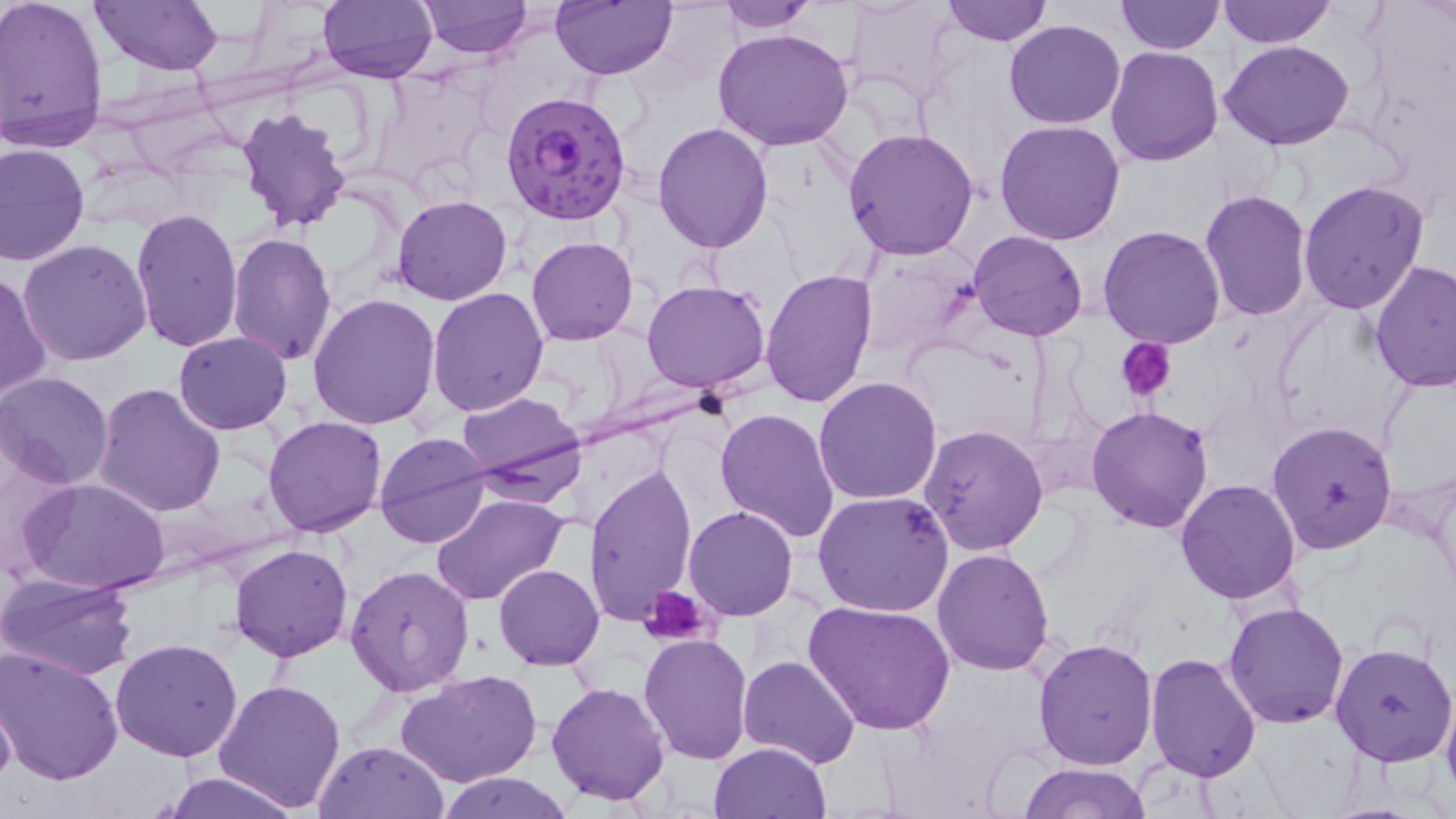

slide-level diagnosis = Plasmodium falciparum
stain = May-Grünwald-Giemsa
image size = 1456×819 pixels
platelet locations = approximate bounding boxes as named x1/y1/x2/y2 corners in pixels: (x1=1121, y1=339, x2=1177, y2=400), (x1=640, y1=587, x2=712, y2=645)
uninfected red blood cell locations = approximate bounding boxes as named x1/y1/x2/y2 corners in pixels: (x1=1, y1=0, x2=111, y2=151), (x1=90, y1=0, x2=224, y2=74), (x1=316, y1=0, x2=438, y2=83), (x1=417, y1=0, x2=531, y2=59), (x1=551, y1=0, x2=675, y2=80), (x1=717, y1=0, x2=820, y2=32), (x1=940, y1=0, x2=1053, y2=47), (x1=1113, y1=0, x2=1228, y2=54), (x1=1216, y1=0, x2=1335, y2=48), (x1=844, y1=2, x2=962, y2=104), (x1=1003, y1=18, x2=1126, y2=129), (x1=713, y1=27, x2=857, y2=152), (x1=1219, y1=40, x2=1356, y2=150), (x1=1105, y1=45, x2=1224, y2=166), (x1=280, y1=75, x2=384, y2=166), (x1=235, y1=108, x2=353, y2=234), (x1=995, y1=118, x2=1127, y2=245), (x1=653, y1=120, x2=777, y2=252), (x1=843, y1=127, x2=981, y2=261), (x1=0, y1=142, x2=91, y2=265), (x1=1298, y1=179, x2=1431, y2=314), (x1=1199, y1=188, x2=1313, y2=324), (x1=390, y1=195, x2=515, y2=305), (x1=130, y1=207, x2=245, y2=353), (x1=1097, y1=224, x2=1227, y2=349), (x1=227, y1=231, x2=337, y2=364), (x1=968, y1=231, x2=1089, y2=341), (x1=527, y1=237, x2=637, y2=347), (x1=18, y1=239, x2=153, y2=366), (x1=853, y1=243, x2=985, y2=360), (x1=1370, y1=260, x2=1456, y2=393), (x1=759, y1=268, x2=879, y2=407), (x1=0, y1=270, x2=51, y2=404), (x1=642, y1=280, x2=769, y2=392), (x1=426, y1=286, x2=549, y2=416), (x1=307, y1=293, x2=442, y2=431), (x1=174, y1=330, x2=292, y2=434), (x1=0, y1=372, x2=115, y2=489), (x1=813, y1=376, x2=944, y2=504), (x1=95, y1=383, x2=227, y2=519), (x1=455, y1=392, x2=585, y2=495), (x1=1087, y1=404, x2=1217, y2=533), (x1=714, y1=407, x2=840, y2=544), (x1=262, y1=416, x2=386, y2=538), (x1=1268, y1=420, x2=1398, y2=554), (x1=919, y1=423, x2=1048, y2=556), (x1=373, y1=431, x2=491, y2=548), (x1=585, y1=463, x2=697, y2=628), (x1=18, y1=477, x2=172, y2=596), (x1=1176, y1=478, x2=1303, y2=605), (x1=812, y1=488, x2=956, y2=616), (x1=430, y1=493, x2=569, y2=607), (x1=684, y1=505, x2=798, y2=620), (x1=228, y1=543, x2=353, y2=663), (x1=932, y1=548, x2=1055, y2=675), (x1=494, y1=563, x2=604, y2=671), (x1=344, y1=565, x2=475, y2=698), (x1=0, y1=573, x2=139, y2=681), (x1=804, y1=599, x2=957, y2=737), (x1=1222, y1=602, x2=1350, y2=729), (x1=639, y1=632, x2=754, y2=763), (x1=110, y1=636, x2=243, y2=761), (x1=1032, y1=638, x2=1158, y2=771), (x1=1329, y1=643, x2=1456, y2=768), (x1=0, y1=645, x2=124, y2=786), (x1=1143, y1=653, x2=1262, y2=782), (x1=737, y1=656, x2=860, y2=770), (x1=397, y1=670, x2=541, y2=789), (x1=212, y1=676, x2=350, y2=813), (x1=547, y1=681, x2=670, y2=805), (x1=1, y1=689, x2=17, y2=796), (x1=1441, y1=690, x2=1456, y2=806), (x1=316, y1=740, x2=448, y2=819), (x1=708, y1=742, x2=833, y2=818), (x1=1016, y1=762, x2=1150, y2=819), (x1=161, y1=771, x2=303, y2=819), (x1=434, y1=773, x2=574, y2=819)
modality = optical microscopy
Plasmodium falciparum-infected red blood cell locations = approximate bounding boxes as named x1/y1/x2/y2 corners in pixels: (x1=501, y1=91, x2=632, y2=226)
field of view = one of a larger specimen
preparation = thin blood smear
magnification = 1000x